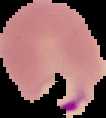
Summary:
  - Image size: 106×118 pixels
  - Image type: segmented cell region with the area outside set to black
  - Malaria status: parasitized
  - Preparation: thin blood film